Assess this cell for malaria.
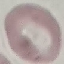
It is uninfected.

Giemsa stain. Acquired by smartphone through the microscope eyepiece. Automatically extracted cell patch, resized to 64 × 64 pixels. Thin smear of blood.